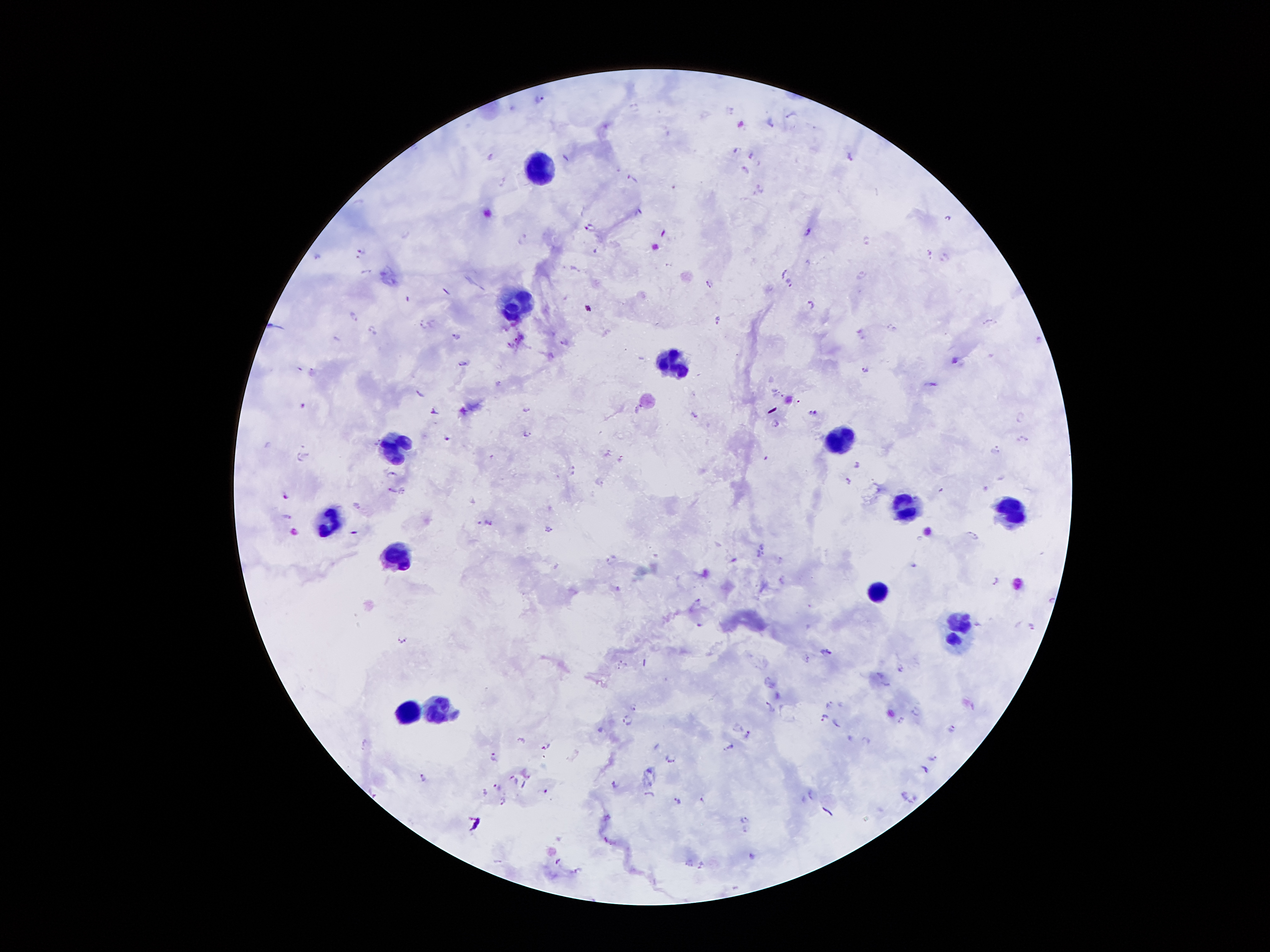

Approximate centers as (x, y) in pixels. Leukocyte locations: (540, 168), (522, 302), (671, 362), (839, 439), (395, 444), (904, 503), (1014, 509), (330, 518), (393, 560), (877, 589), (958, 639), (439, 704), (409, 714). Plasmodium parasite locations: (540, 98), (728, 108), (791, 113), (704, 114), (770, 120), (741, 124), (735, 149), (850, 155), (751, 156), (491, 157), (745, 171), (632, 179), (759, 190), (949, 218), (590, 226), (808, 231), (522, 238), (866, 242), (360, 249), (928, 252), (315, 255), (946, 255), (783, 272), (364, 274), (862, 274), (789, 281), (709, 282), (811, 303), (352, 316), (716, 319), (989, 320), (433, 322), (420, 326), (892, 326), (371, 329), (861, 333), (456, 337), (1039, 338), (562, 340), (553, 355), (954, 357), (463, 361), (864, 368), (311, 372), (499, 382), (931, 382), (421, 392), (303, 403), (528, 409), (432, 413), (813, 413), (696, 414), (1022, 419), (775, 422), (525, 433), (447, 438), (1023, 439), (996, 449), (609, 452), (301, 456), (620, 459), (855, 462), (571, 469), (391, 474), (849, 481), (599, 482), (391, 488), (403, 490), (286, 496), (287, 514), (489, 525), (548, 530), (971, 535), (761, 553), (734, 559), (609, 560), (779, 560), (781, 578), (994, 580), (618, 587), (698, 599), (1050, 600), (699, 624), (977, 624), (1030, 624), (401, 638), (825, 652), (807, 659), (619, 665), (901, 668), (831, 704), (634, 705), (771, 705), (915, 711), (824, 716), (627, 720), (836, 722), (899, 722), (950, 727), (747, 734), (522, 739), (868, 740), (546, 745), (729, 745), (492, 756), (935, 757), (669, 759), (923, 768), (527, 775), (422, 776), (512, 777), (613, 783), (499, 785), (524, 785), (545, 791), (483, 792), (904, 793), (648, 794), (811, 795), (502, 799), (677, 800), (702, 800), (743, 819), (747, 830), (751, 855), (556, 860), (689, 863), (700, 866), (579, 870). Photographed through the microscope eyepiece with a smartphone camera. Thick blood film. One field from this slide. 100x magnification. Patient malaria status: positive for Plasmodium falciparum. Giemsa-stained preparation. Image is 1270×952 pixels.